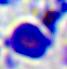

magnification = 400x
identification = leukocyte
modality = photomicrograph